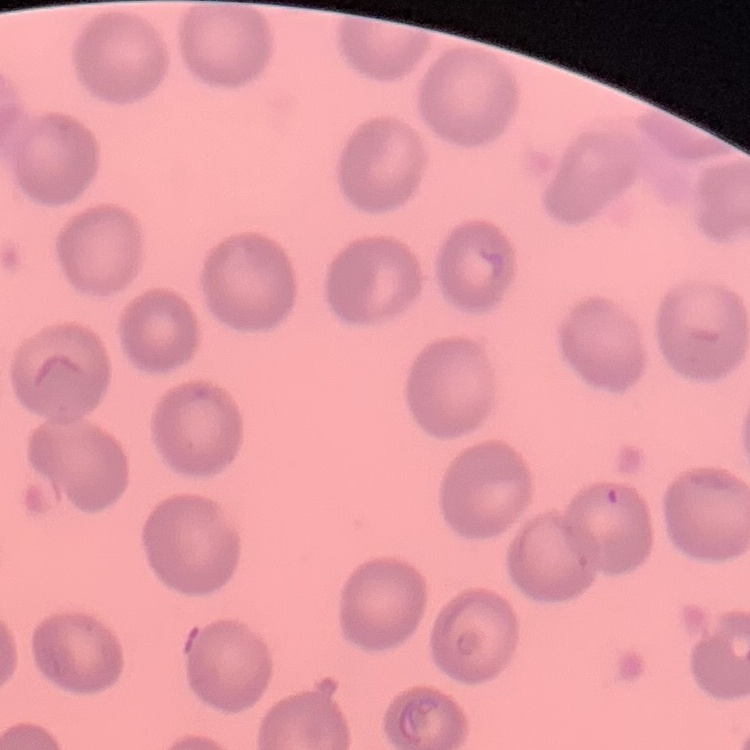
red_blood_cell_morphology: no rouleaux formation
stain: Field's or Giemsa
image_type: one tile cut from a larger photomicrograph
preparation: thin blood film